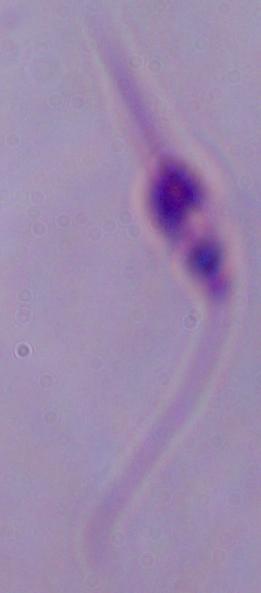
Summary:
  - Modality: photomicrograph
  - Magnification: 1000x
  - Identification: Leishmania